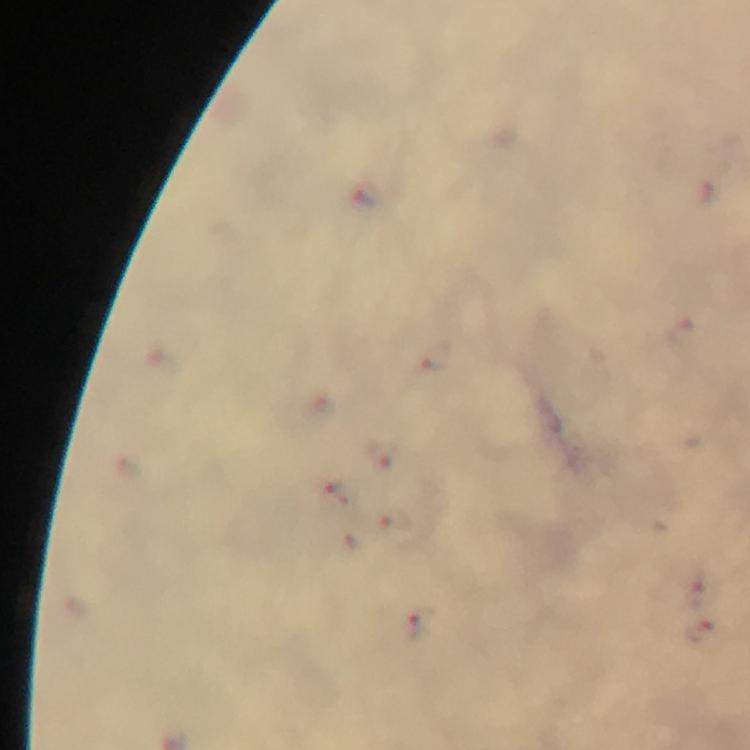

context = from a malaria diagnostic workup
stain = Giemsa
cropped from = a single field of view
immersion oil = applied
malaria parasite locations = approximate centers as (x, y) in pixels: (380, 458), (340, 493), (395, 525), (353, 547), (695, 590), (418, 624), (700, 631)
preparation = thick blood film
image size = 750×750 pixels
capture = smartphone photograph through a microscope
magnification = 100x